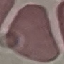
result: negative for malaria parasites
stain: Giemsa
capture: smartphone through the microscope eyepiece
image_type: cell patch, automatically extracted from a larger field of view and resized to 64 × 64 pixels
preparation: thin blood smear